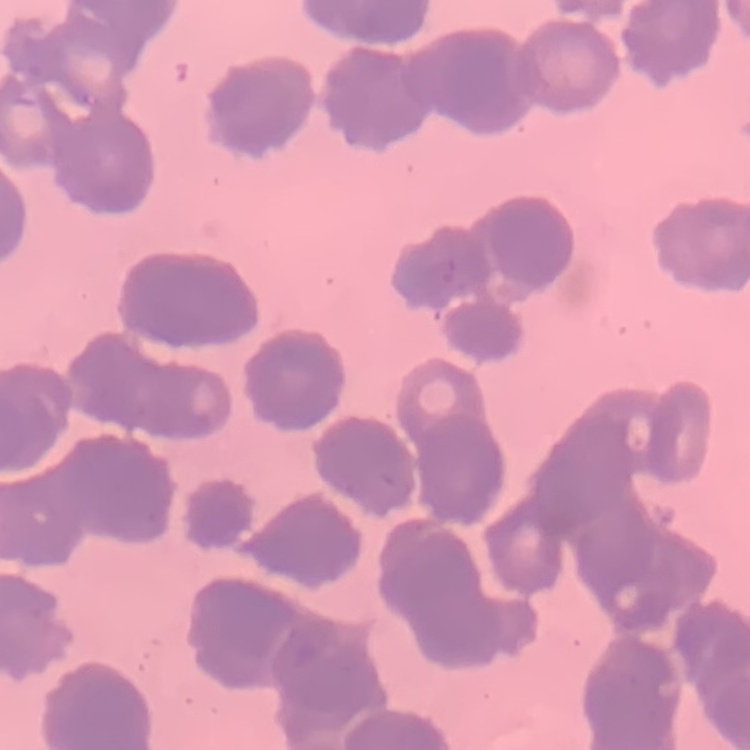

{
  "red_blood_cell_morphology": "rouleaux formation",
  "stain": "Field's or Giemsa",
  "image_type": "one tile cut from a larger photomicrograph",
  "preparation": "thin peripheral smear"
}